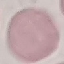 Malaria status: uninfected. Thin blood smear. Acquired by smartphone through the microscope eyepiece. Giemsa-stained preparation. Automatically extracted cell patch, resized to 64 × 64 pixels.